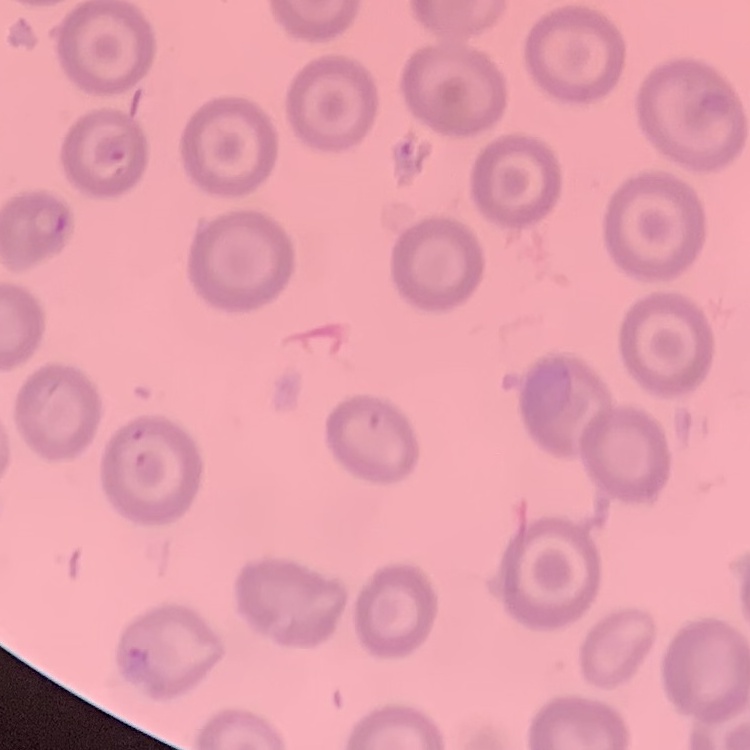 The red blood cells exhibit no rouleaux formation. Square crop of a larger photomicrograph. Thin blood film. Field's or Giemsa stain.